Assess this cell for malaria.
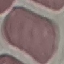
Uninfected.

Summary:
  - Image type: cell patch, automatically extracted from a larger field of view and resized to 64 × 64 pixels
  - Capture: smartphone through the microscope eyepiece
  - Preparation: thin smear
  - Stain: Giemsa